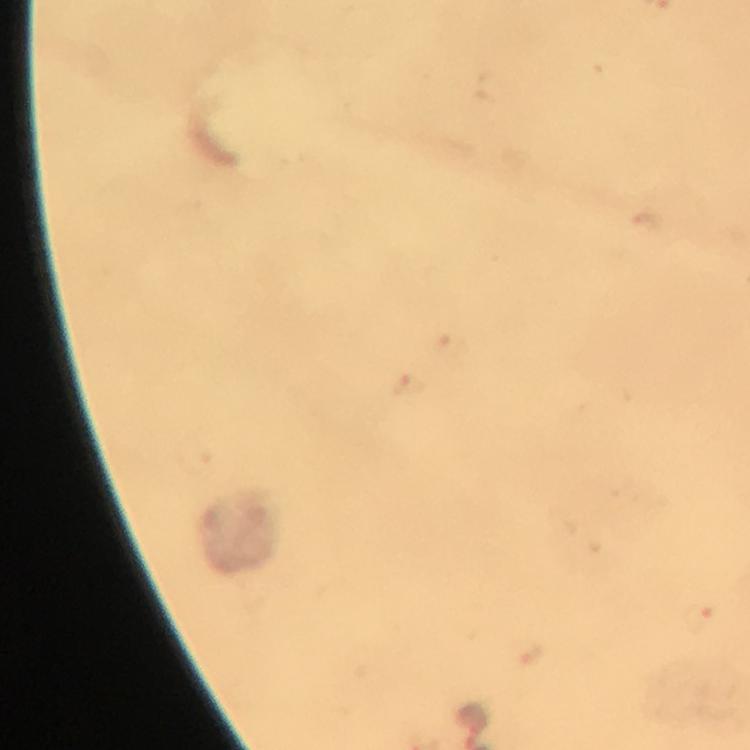

{
  "preparation": "thick blood film",
  "cropped_from": "one field of view",
  "stain": "Giemsa",
  "image_size": "750×750 pixels",
  "immersion_oil": "used",
  "plasmodium_parasite_locations": "approximate object centers, in pixels from the top-left corner: (x=453, y=347), (x=410, y=387), (x=700, y=620), (x=471, y=718)",
  "context": "from a malaria diagnostic workup",
  "capture": "smartphone camera through the microscope",
  "magnification": "100x"
}